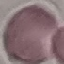 Result: no malaria parasites seen. Giemsa-stained preparation. Automatically extracted cell patch, resized to 64 × 64 pixels. Thin blood smear. Acquired by smartphone through the microscope eyepiece.